Describe the morphology of the red blood cells.
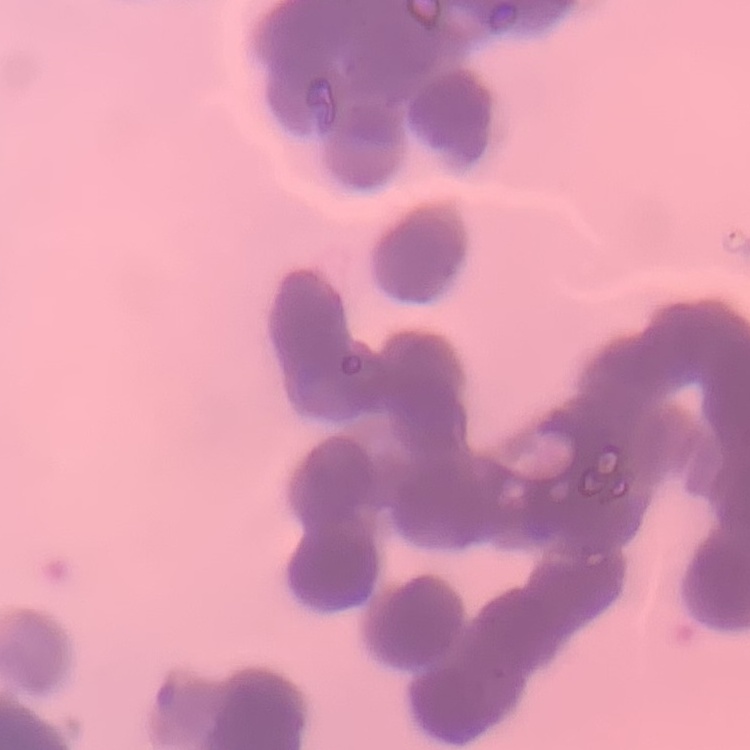
They show rouleaux formation.

Square crop of a larger photomicrograph. Field's or Giemsa stain. Thin peripheral smear.